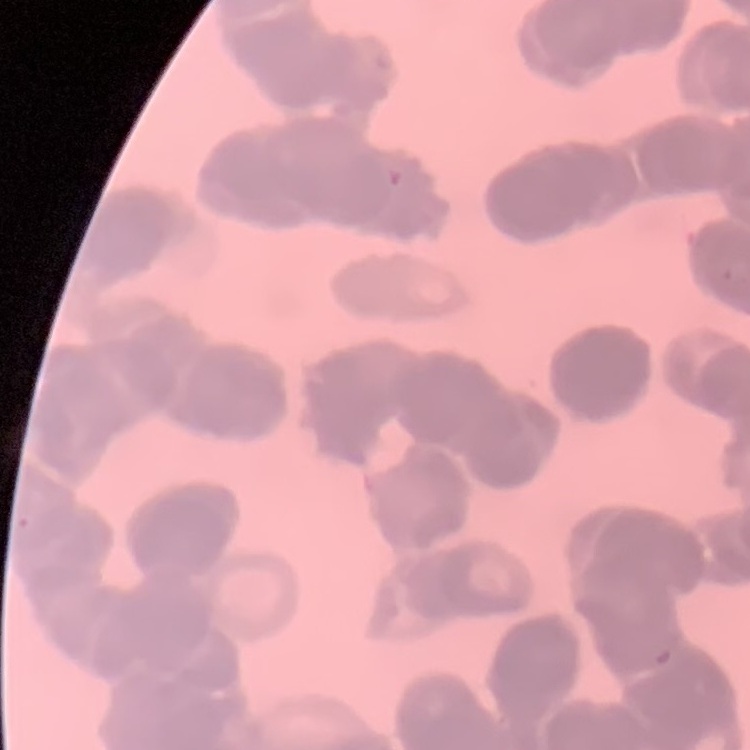

The erythrocytes exhibit rouleaux formation. Thin peripheral smear. One tile cut from a larger photomicrograph. Field's or Giemsa stain.